State the preparation type.
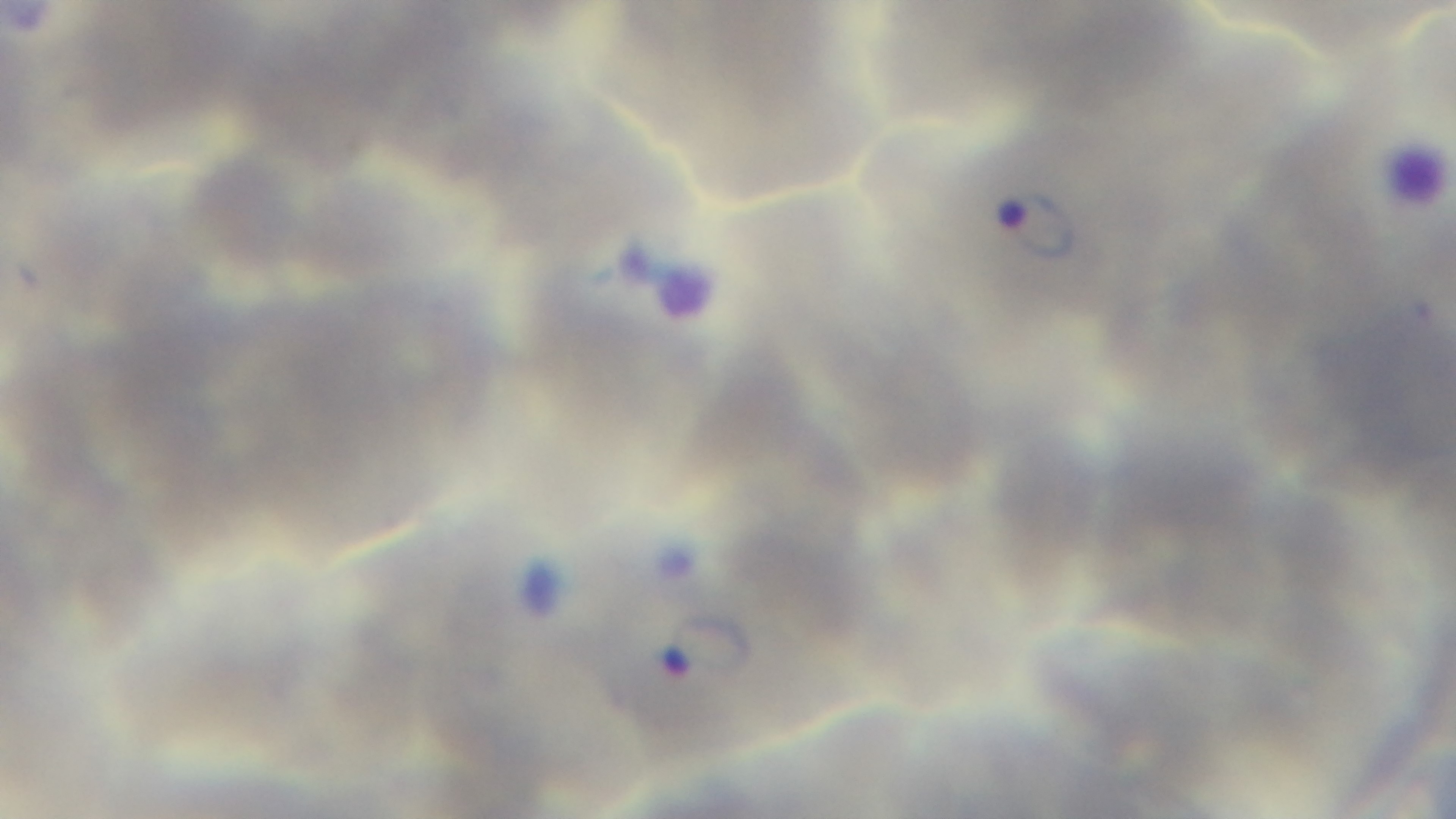

Thin.

Summary:
  - Field of view: single
  - Objective: 100x oil immersion
  - Capture: mounted 4K digital camera
  - Modality: light microscopy
  - Stain: Giemsa
  - Malaria status: positive